Identify the blood parasite species.
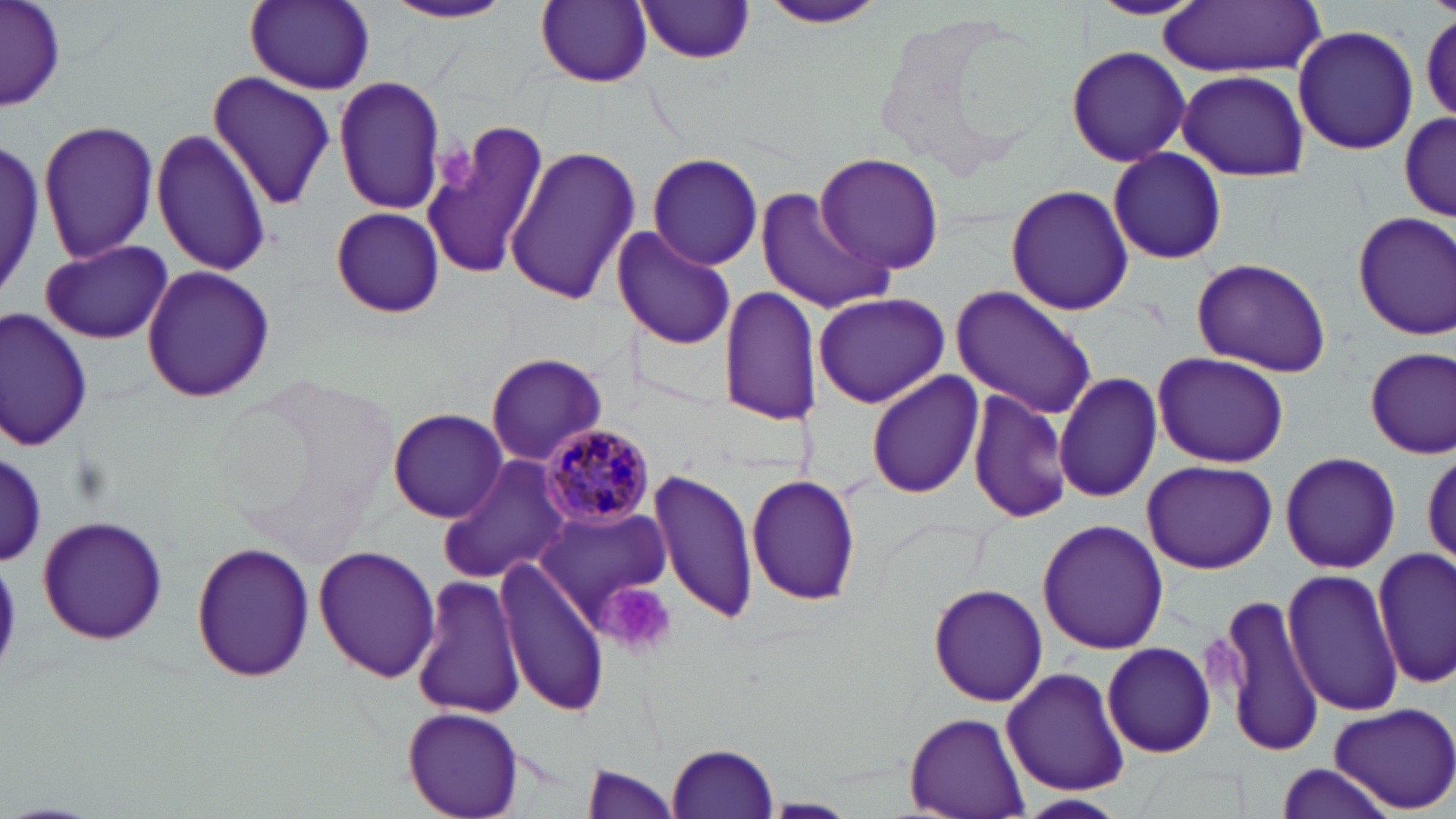
Plasmodium malariae.

image_size: 1456×819 pixels
magnification: 1000x
stain: May-Grünwald-Giemsa
uninfected_red_blood_cell_locations: 'approximate bounding boxes as (x1,y1)-(x2,y2) corner pairs in pixels: (3,0)-(66,111), (244,0)-(374,92), (535,0)-(652,88), (1082,0)-(1205,20), (384,1)-(516,25), (757,1)-(889,31), (633,2)-(758,64), (1156,2)-(1324,76), (1421,10)-(1456,122), (1292,25)-(1420,155), (1066,44)-(1191,168), (1174,68)-(1311,182), (205,69)-(336,213), (333,76)-(447,214), (1398,109)-(1453,224), (420,117)-(550,284), (39,120)-(158,263), (151,129)-(270,276), (0,134)-(46,299), (505,145)-(639,308), (1106,148)-(1229,266), (646,152)-(763,269), (814,153)-(945,277), (1004,184)-(1135,318), (754,187)-(894,316), (331,207)-(444,319), (1353,210)-(1456,342), (612,225)-(737,351), (40,239)-(171,345), (1191,257)-(1331,376), (141,265)-(276,403), (718,285)-(823,427), (950,286)-(1099,420), (813,292)-(950,409), (1,309)-(92,452), (1364,346)-(1455,458), (1152,353)-(1289,466), (484,354)-(609,467), (864,371)-(983,499), (1053,371)-(1161,503), (967,387)-(1072,525), (388,408)-(509,522), (2,451)-(46,564), (1279,452)-(1401,575), (437,456)-(572,587), (1140,460)-(1280,572), (647,468)-(756,626), (746,473)-(863,609), (536,507)-(672,625), (33,515)-(171,646), (1035,518)-(1170,654), (190,540)-(315,685), (312,544)-(441,685), (1374,550)-(1455,688), (495,556)-(610,717), (1284,568)-(1402,716), (410,572)-(525,723), (927,583)-(1049,706), (1215,592)-(1326,759), (1101,642)-(1215,758), (1001,667)-(1132,796), (1327,702)-(1456,814), (403,705)-(523,817), (904,710)-(1031,817), (668,742)-(781,817), (1273,762)-(1395,819), (580,766)-(685,818), (1011,793)-(1129,817)'
plasmodium_malariae_infected_red_blood_cell_locations: 'approximate bounding boxes as (x1,y1)-(x2,y2) corner pairs in pixels: (539,420)-(656,528)'
field_of_view: single
platelet_locations: 'approximate bounding boxes as (x1,y1)-(x2,y2) corner pairs in pixels: (429,136)-(485,200), (601,583)-(677,657)'
preparation: thin blood film
modality: optical microscopy